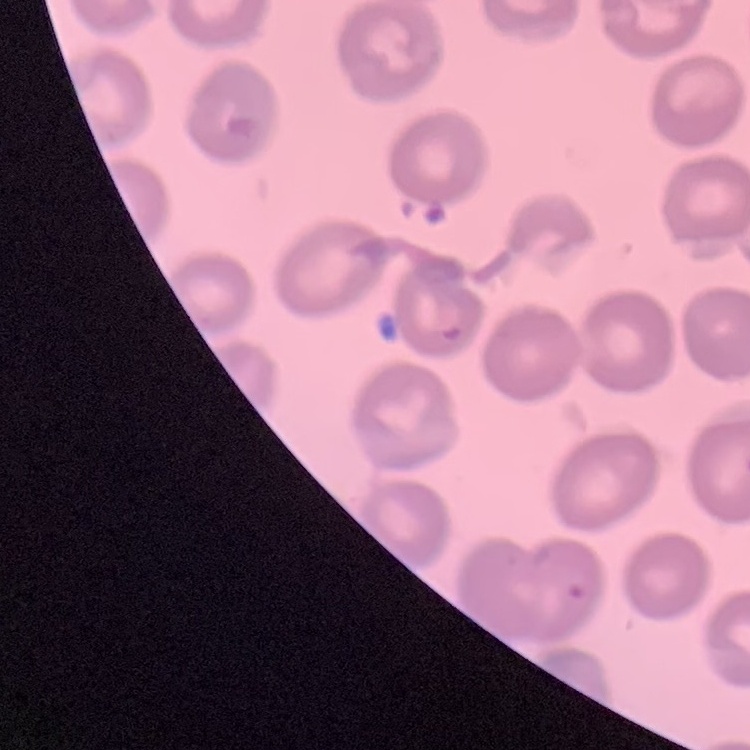
red blood cell morphology = no rouleaux formation
preparation = thin peripheral smear
stain = Field's or Giemsa
image type = square crop of a larger photomicrograph